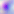

magnification = 400x
identification = Toxoplasma gondii
modality = photomicrograph